State which parasite is depicted.
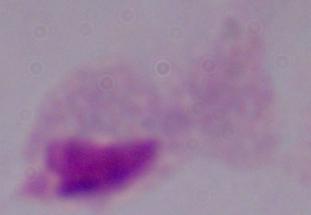
A trichomonad.

Photomicrograph. 1000x magnification.